Locate and identify every blood parasite.
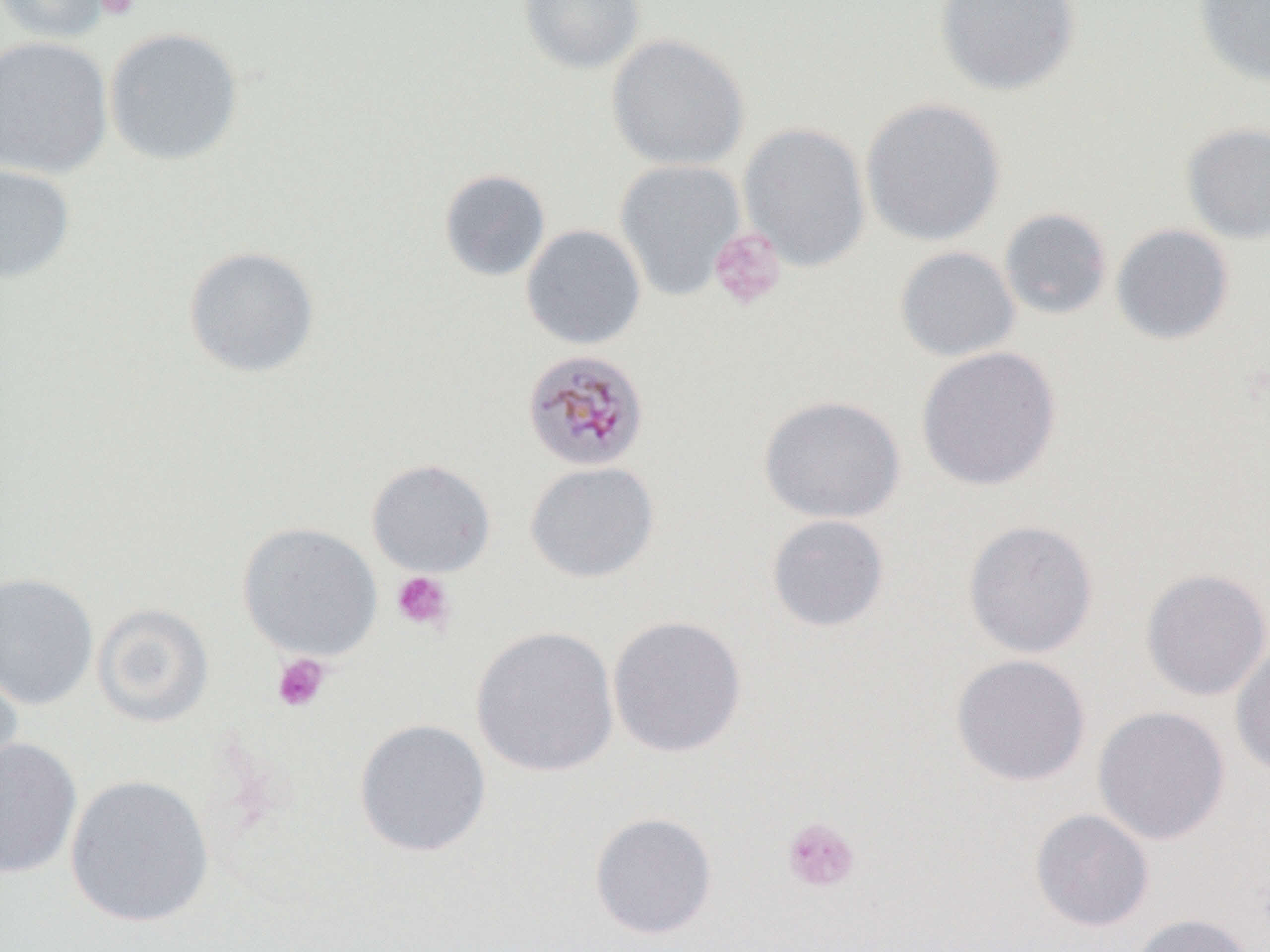
Approximate bounding boxes as [x1, y1, x2, y2] in pixels.
Plasmodium malariae-infected red blood cells: [521, 348, 649, 473].
No Plasmodium falciparum, Plasmodium ovale, Plasmodium vivax, Babesia divergens, or Trypanosoma brucei observed.

Platelet locations: [94, 0, 140, 20], [708, 227, 787, 311], [390, 571, 455, 633], [271, 653, 332, 712], [782, 816, 861, 893]. Uninfected red blood cell locations: [1, 0, 113, 44], [518, 0, 645, 74], [934, 0, 1081, 96], [1193, 0, 1270, 88], [103, 27, 244, 166], [606, 33, 749, 170], [0, 35, 113, 179], [860, 97, 1007, 246], [738, 122, 871, 272], [1181, 122, 1270, 245], [614, 159, 746, 301], [0, 162, 76, 284], [439, 169, 551, 281], [999, 208, 1113, 320], [1111, 223, 1235, 345], [521, 224, 646, 350], [894, 245, 1020, 362], [183, 246, 320, 378], [916, 345, 1062, 491], [758, 394, 906, 524], [367, 459, 496, 577], [524, 460, 659, 583], [766, 514, 890, 632], [963, 519, 1099, 659], [238, 522, 382, 661], [1140, 568, 1270, 701], [0, 572, 99, 710], [92, 603, 214, 728], [607, 614, 748, 758], [471, 625, 619, 778], [1231, 642, 1270, 778], [951, 654, 1091, 787], [0, 659, 23, 791], [1092, 705, 1230, 845], [354, 718, 491, 858], [0, 736, 82, 879], [64, 774, 215, 928], [1029, 808, 1154, 932], [589, 812, 718, 939], [1128, 913, 1256, 952]. Slide-level diagnosis: Plasmodium malariae. Thin blood film. Captured at 1000x magnification. Image is 1270×952 pixels. Light microscopy. One field of a larger specimen.